Report the malaria status of this cell.
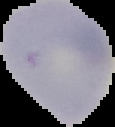

It is uninfected.

{
  "preparation": "thin blood film",
  "image_type": "segmented cell region on a black background",
  "image_size": "115×127 pixels"
}